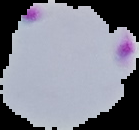
Summary:
  - Image size: 139×130 pixels
  - Preparation: thin blood film
  - Image type: segmented cell region with the area outside set to black
  - Result: malaria parasites detected